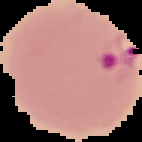
Malaria status: parasitized. The area outside the segmented cell region is set to black. Image is 142×142 pixels. From a thin blood smear.